Describe the morphology of the erythrocytes.
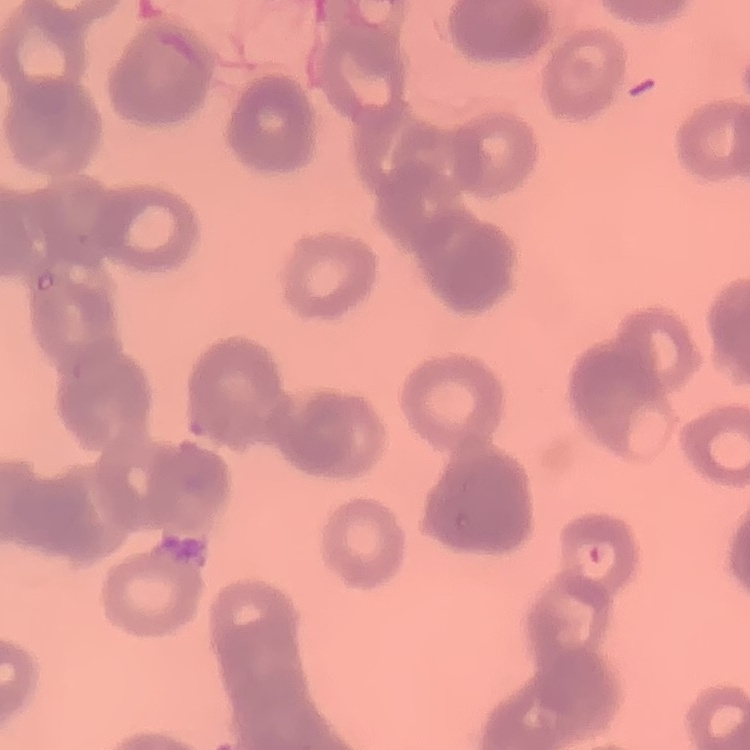
Rouleaux formation.

Thin blood smear. Square crop of a larger photomicrograph. Stained with either Field's or Giemsa.